Classify this cell by malaria status.
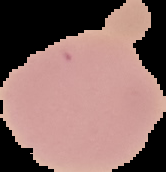
Uninfected.

Summary:
  - Image type: segmented cell region on a black background
  - Preparation: thin blood smear
  - Image size: 166×172 pixels